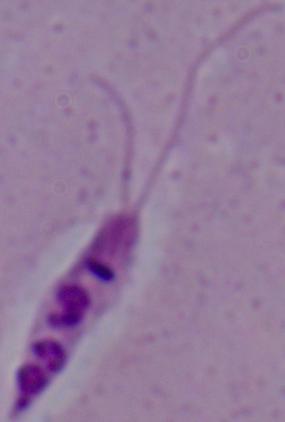 1000x magnification. Photomicrograph. A Leishmania parasite is seen.